Identify the cell.
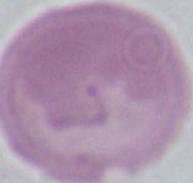

This is an erythrocyte.

Summary:
  - Magnification: 1000x
  - Modality: micrograph